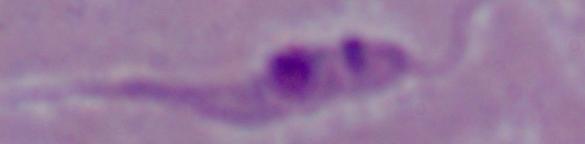
Summary:
  - Modality: photomicrograph
  - Magnification: 1000x
  - Identification: Leishmania